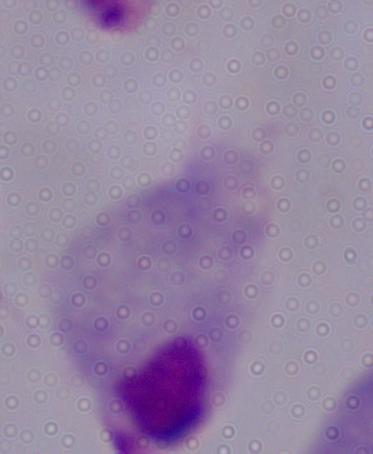
Captured at 1000x magnification. Photomicrograph. A trichomonad is shown.